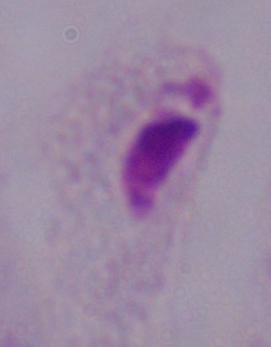

Captured at 1000x magnification. A trichomonad is seen. Photomicrograph.